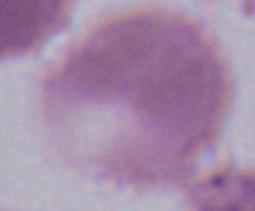

A red blood cell is shown. Micrograph. Captured at 1000x magnification.